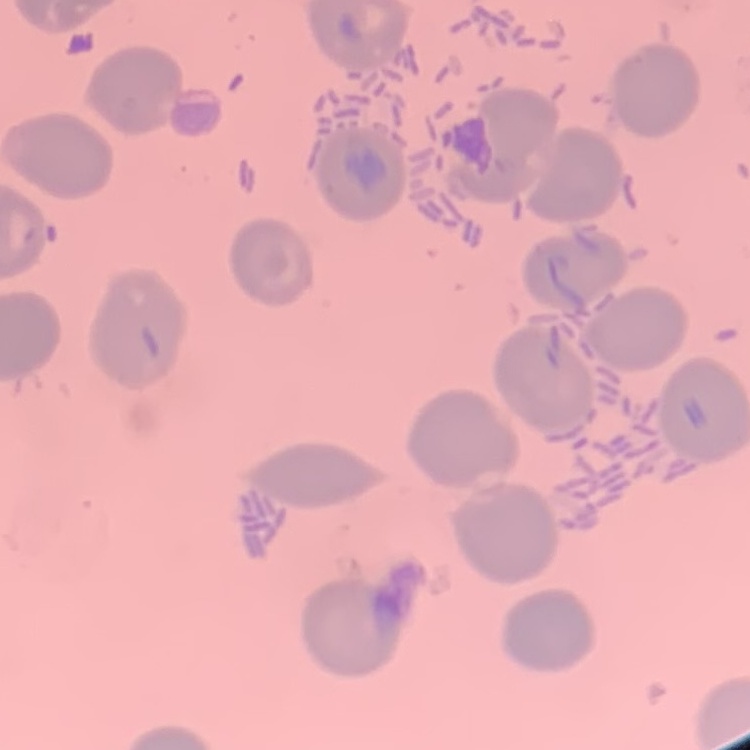 The erythrocytes show no rouleaux formation. Square crop of a larger photomicrograph. Stained with either Field's or Giemsa. Thin peripheral smear.